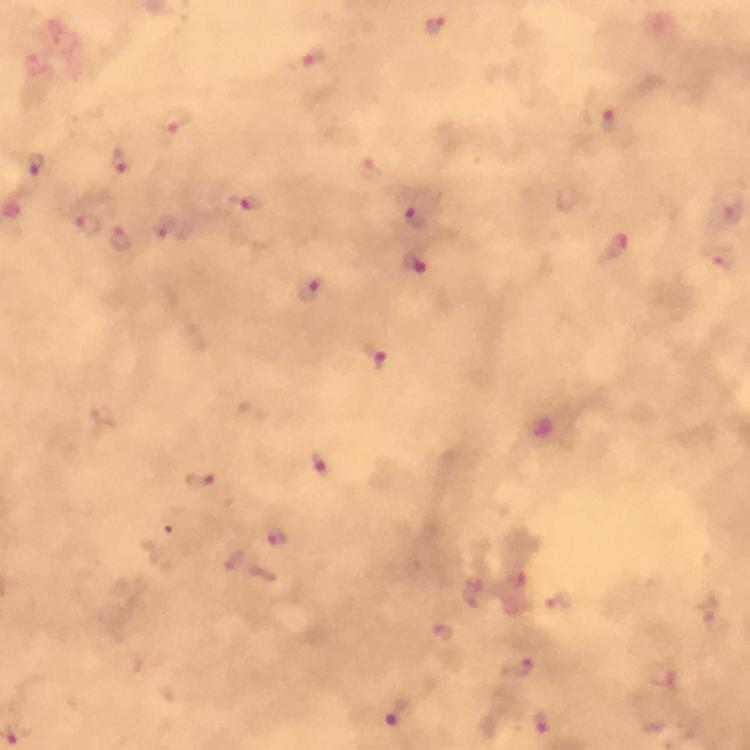
Approximate centers as [x, y] in pixels. Plasmodium parasite locations: [436, 27], [313, 59], [609, 120], [174, 122], [121, 160], [36, 165], [246, 201], [725, 208], [415, 209], [87, 226], [174, 229], [121, 239], [618, 249], [415, 260], [311, 287], [379, 357], [321, 465], [200, 481], [276, 538], [475, 592], [559, 601], [445, 633], [517, 666], [661, 678], [396, 712], [540, 721]. Cropped region of a single field of view. Giemsa-stained preparation. Image is 750×750 pixels. 100x magnification. Thick blood film. Immersion oil was used. Smartphone photograph taken through a microscope. From a diagnostic examination for malaria.